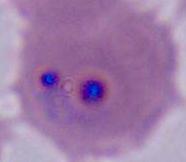
Summary:
  - Magnification: 400x or 1000x
  - Modality: micrograph
  - Identification: Plasmodium